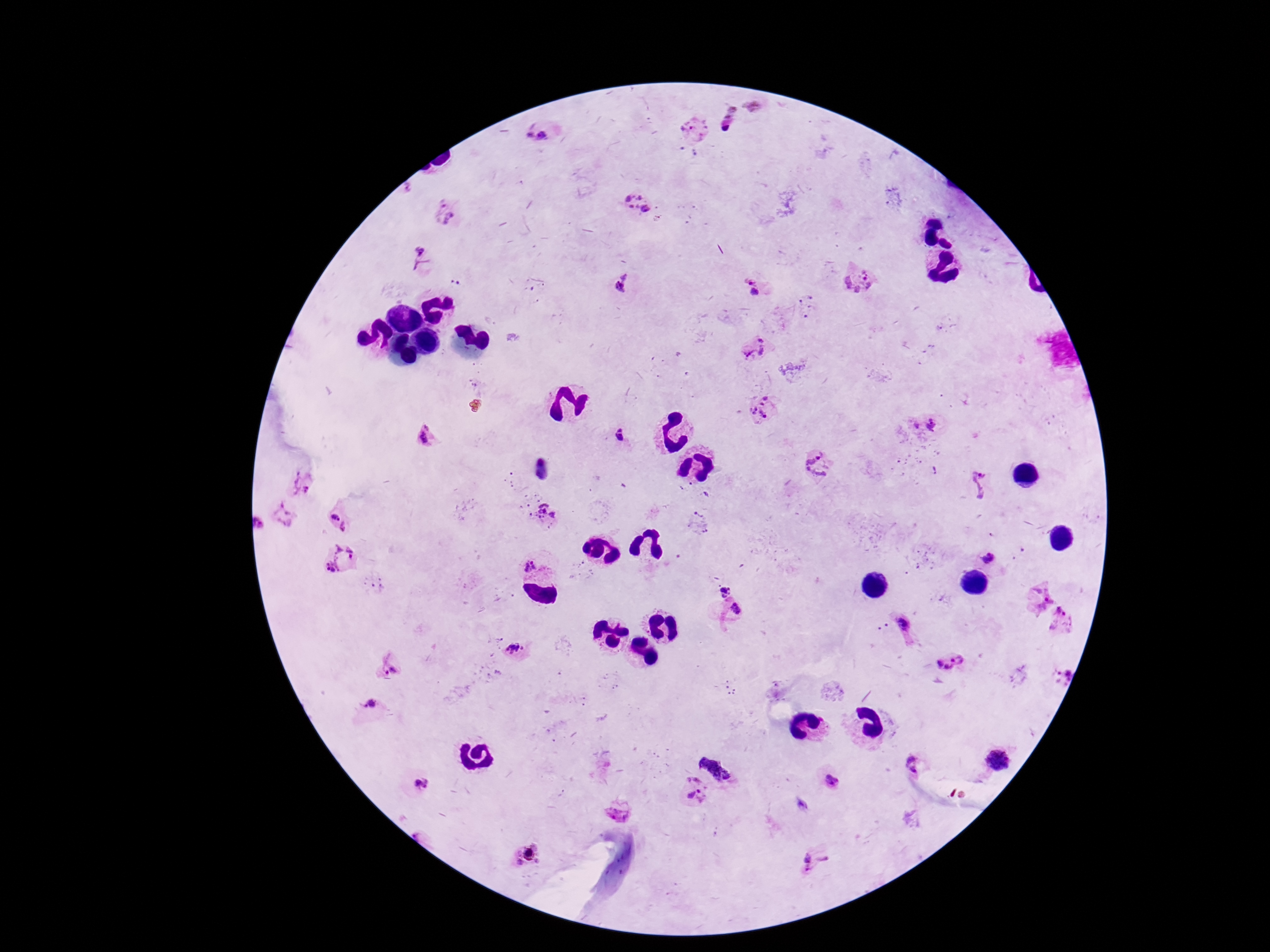

preparation = thick blood smear
image size = 1270×952 pixels
Plasmodium parasite locations = approximate centers as (x, y) in pixels: (693, 129), (539, 134), (638, 207), (445, 212), (419, 261), (861, 279), (622, 285), (750, 287), (756, 347), (764, 408), (933, 425), (916, 426), (426, 435), (620, 435), (819, 466), (301, 481), (979, 483), (543, 513), (283, 515), (335, 517), (700, 523), (258, 524), (347, 527), (989, 558), (340, 560), (529, 564), (1035, 597), (1063, 619), (903, 622), (515, 651), (952, 662), (389, 667), (1060, 672), (370, 706), (725, 745), (999, 760), (912, 762), (831, 782), (422, 784), (696, 790), (620, 808), (530, 853), (816, 860)
patient malaria status = positive
field of view = one from this slide
capture = smartphone camera through the microscope eyepiece
stain = Giemsa
magnification = 100x